Point out leukocytes.
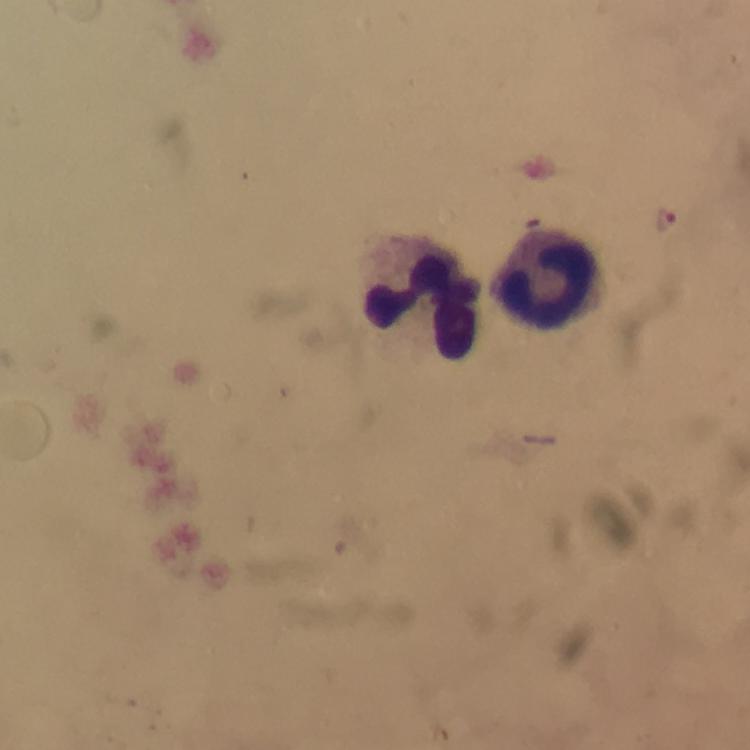

Approximate centers as (x, y) in pixels.
Leukocytes: (551, 281), (423, 305).

Summary:
  - Plasmodium parasite locations: (666, 218)
  - Image size: 750×750 pixels
  - Cropped from: one field of view
  - Magnification: 100x
  - Context: from a diagnostic examination for malaria
  - Immersion oil: applied
  - Preparation: thick blood smear
  - Stain: Giemsa
  - Capture: smartphone camera through the microscope